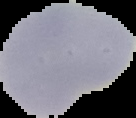
result = no Plasmodium parasites detected
image size = 136×118 pixels
preparation = thin blood smear
image type = segmented cell region on a black background